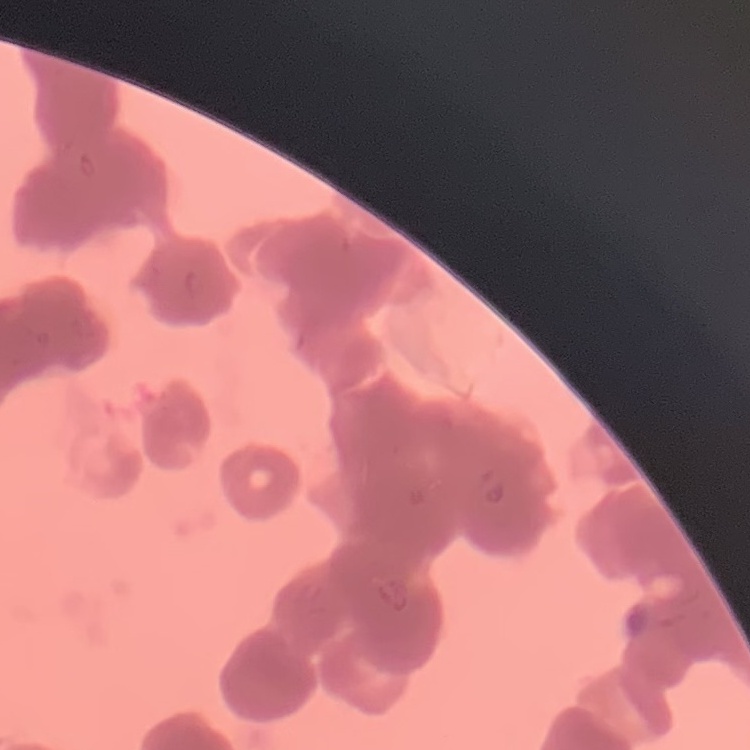 The red blood cells show rouleaux formation. Thin peripheral smear. Stained with either Field's or Giemsa. One tile cut from a larger photomicrograph.